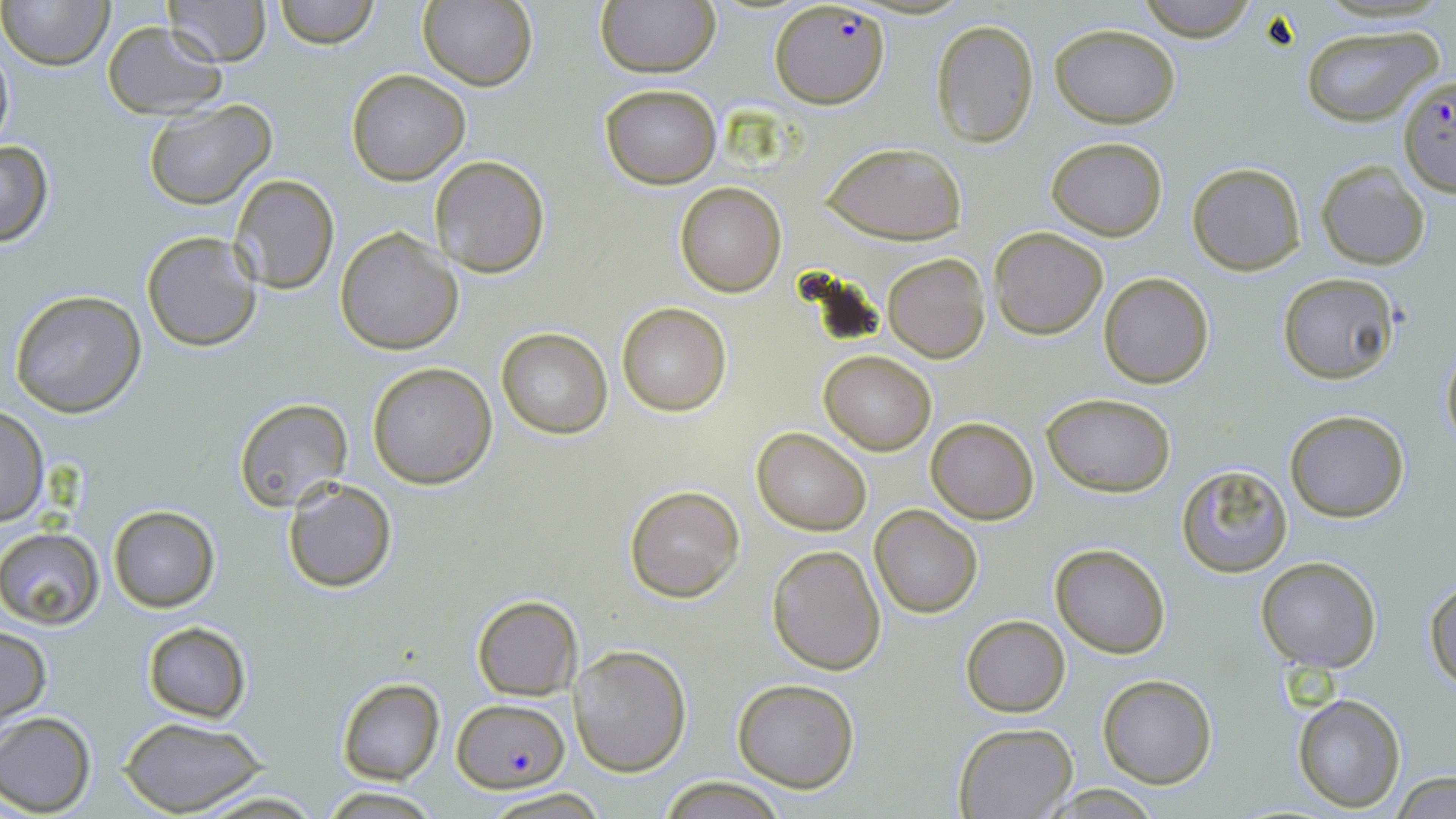

Summary:
  - Coordinate format: approximate bounding boxes as (x1, y1, x2, y2) in pixels
  - Plasmodium falciparum-infected red blood cell locations: (770, 4, 891, 111), (1398, 75, 1456, 195), (453, 697, 569, 792)
  - Uninfected red blood cell locations: (1, 0, 115, 71), (164, 0, 270, 66), (275, 0, 377, 48), (420, 0, 538, 91), (1135, 0, 1259, 41), (595, 1, 719, 76), (929, 18, 1040, 147), (102, 21, 225, 118), (1298, 23, 1443, 128), (1049, 24, 1180, 127), (0, 35, 15, 162), (345, 68, 471, 185), (599, 83, 722, 189), (142, 101, 277, 210), (1047, 137, 1168, 240), (0, 139, 55, 247), (822, 141, 967, 243), (429, 156, 550, 277), (1317, 160, 1431, 269), (1188, 162, 1306, 275), (229, 174, 340, 294), (675, 182, 787, 296), (335, 226, 462, 355), (989, 226, 1109, 340), (142, 231, 263, 352), (883, 253, 990, 362), (1099, 273, 1214, 389), (1278, 274, 1399, 385), (8, 289, 147, 417), (617, 302, 731, 416), (495, 326, 612, 440), (1439, 341, 1456, 452), (820, 350, 935, 454), (368, 361, 497, 487), (1042, 393, 1176, 496), (234, 398, 354, 515), (0, 407, 48, 527), (1284, 409, 1409, 522), (925, 418, 1039, 524), (751, 426, 871, 535), (1176, 464, 1293, 578), (282, 479, 398, 592), (623, 485, 746, 603), (869, 504, 983, 618), (108, 505, 219, 611), (0, 527, 103, 628), (1049, 542, 1172, 658), (767, 544, 888, 675), (1255, 556, 1382, 673), (1424, 577, 1456, 692), (472, 595, 582, 700), (960, 615, 1070, 716), (142, 621, 250, 723), (1, 626, 50, 722), (570, 644, 691, 775), (1097, 675, 1217, 788), (336, 677, 446, 785), (732, 677, 859, 791), (1292, 693, 1406, 811), (0, 711, 97, 815), (120, 717, 269, 817), (951, 722, 1077, 819), (1390, 772, 1456, 819), (657, 776, 785, 818), (189, 787, 326, 819), (320, 787, 443, 817), (481, 787, 608, 819)
  - Slide-level diagnosis: Plasmodium falciparum
  - Modality: light microscopy
  - Magnification: 1000x
  - Preparation: thin blood smear
  - Stain: May-Grünwald-Giemsa
  - Field of view: single
  - Image size: 1456×819 pixels